Report the malaria status of this cell.
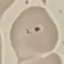
Uninfected.

Acquired by smartphone through the microscope eyepiece. Giemsa-stained preparation. Thin smear of blood. Cell patch, automatically extracted from a larger field of view and resized to 64 × 64 pixels.